Give the extent of all uninfected red blood cells.
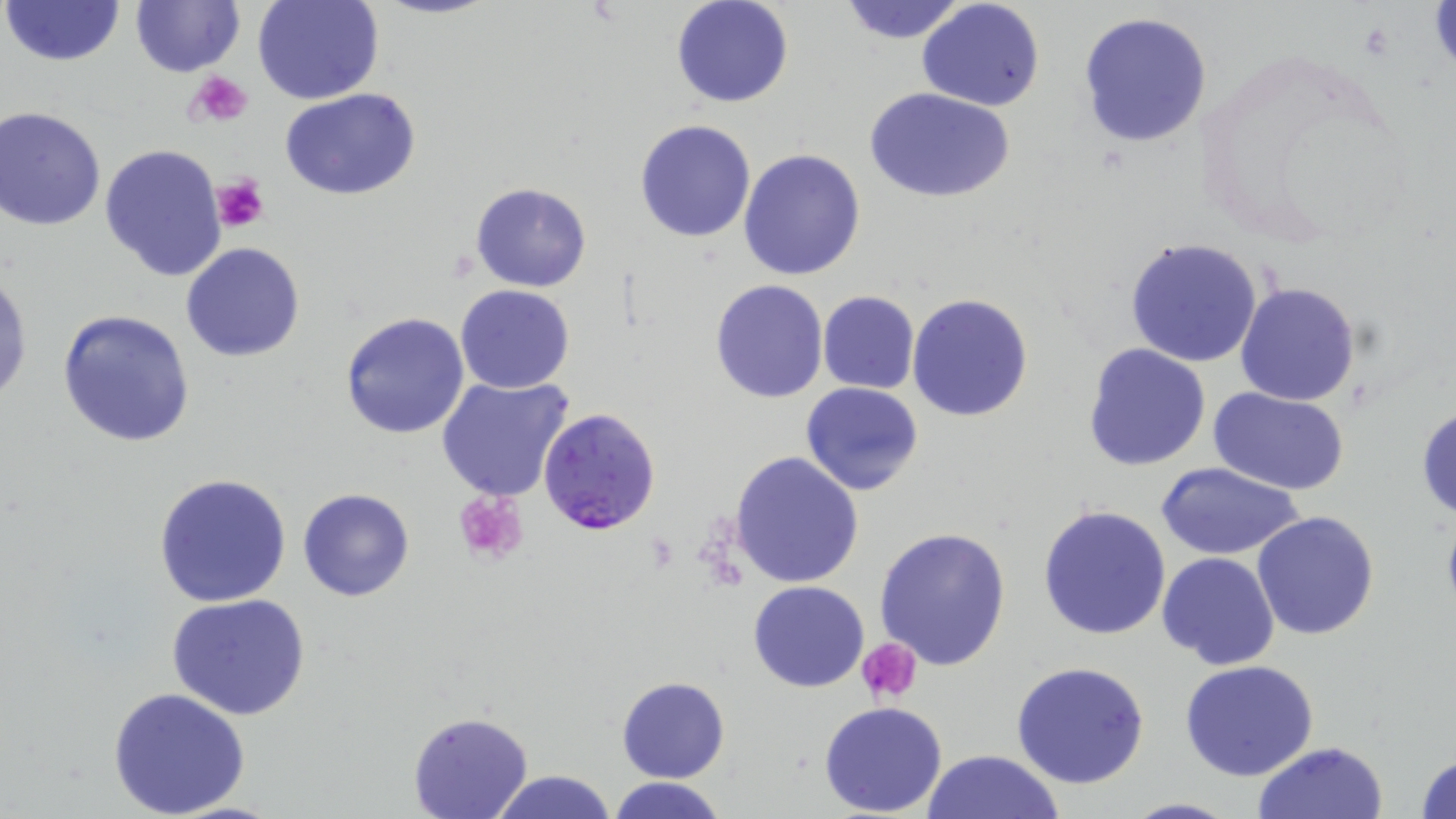
Approximate bounding boxes as (x1, y1, x2, y2) in pixels.
Uninfected red blood cells: (2, 0, 126, 68), (131, 0, 246, 77), (251, 0, 384, 105), (671, 0, 794, 108), (835, 1, 972, 44), (916, 1, 1046, 112), (1078, 13, 1212, 147), (865, 87, 1016, 203), (281, 89, 421, 200), (1, 105, 110, 231), (634, 118, 757, 243), (100, 144, 229, 283), (738, 148, 867, 282), (470, 182, 593, 292), (1122, 237, 1265, 368), (181, 242, 305, 362), (0, 264, 32, 411), (710, 280, 828, 404), (1234, 280, 1362, 405), (456, 285, 575, 394), (817, 290, 920, 394), (907, 294, 1034, 423), (57, 308, 195, 447), (339, 312, 470, 440), (1082, 344, 1211, 471), (436, 376, 576, 504), (801, 381, 923, 495), (1210, 388, 1353, 492), (1415, 403, 1456, 523), (729, 450, 865, 590), (1154, 461, 1305, 562), (152, 474, 293, 608), (297, 488, 414, 601), (1039, 503, 1171, 640), (1252, 511, 1380, 642), (873, 526, 1011, 671), (1158, 551, 1281, 671), (748, 580, 870, 692), (167, 594, 313, 720), (1010, 661, 1150, 788), (1179, 661, 1320, 781), (616, 677, 730, 783), (108, 686, 251, 818), (818, 700, 949, 817), (406, 712, 533, 819), (1250, 741, 1389, 819), (922, 748, 1064, 819), (1412, 750, 1456, 819), (489, 770, 619, 819), (608, 776, 729, 819), (1119, 796, 1240, 818).

Platelet locations: (188, 70, 255, 127), (210, 173, 270, 234), (454, 489, 529, 565), (858, 638, 922, 702). Plasmodium falciparum-infected red blood cell locations: (539, 407, 661, 537). Slide-level diagnosis: Plasmodium falciparum. One field of a larger specimen. May-Grünwald-Giemsa stain. 1000x magnification. Thin blood smear. Image is 1456×819 pixels. Light microscopy.